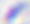

modality = photomicrograph
magnification = 400x
identification = Toxoplasma gondii